Assess this cell for malaria.
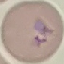

It is parasitized.

{
  "preparation": "thin blood smear",
  "image_type": "cell patch, automatically extracted from a larger field of view and resized to 64 × 64 pixels",
  "capture": "smartphone through the microscope eyepiece",
  "stain": "Giemsa"
}